Locate every Plasmodium parasite.
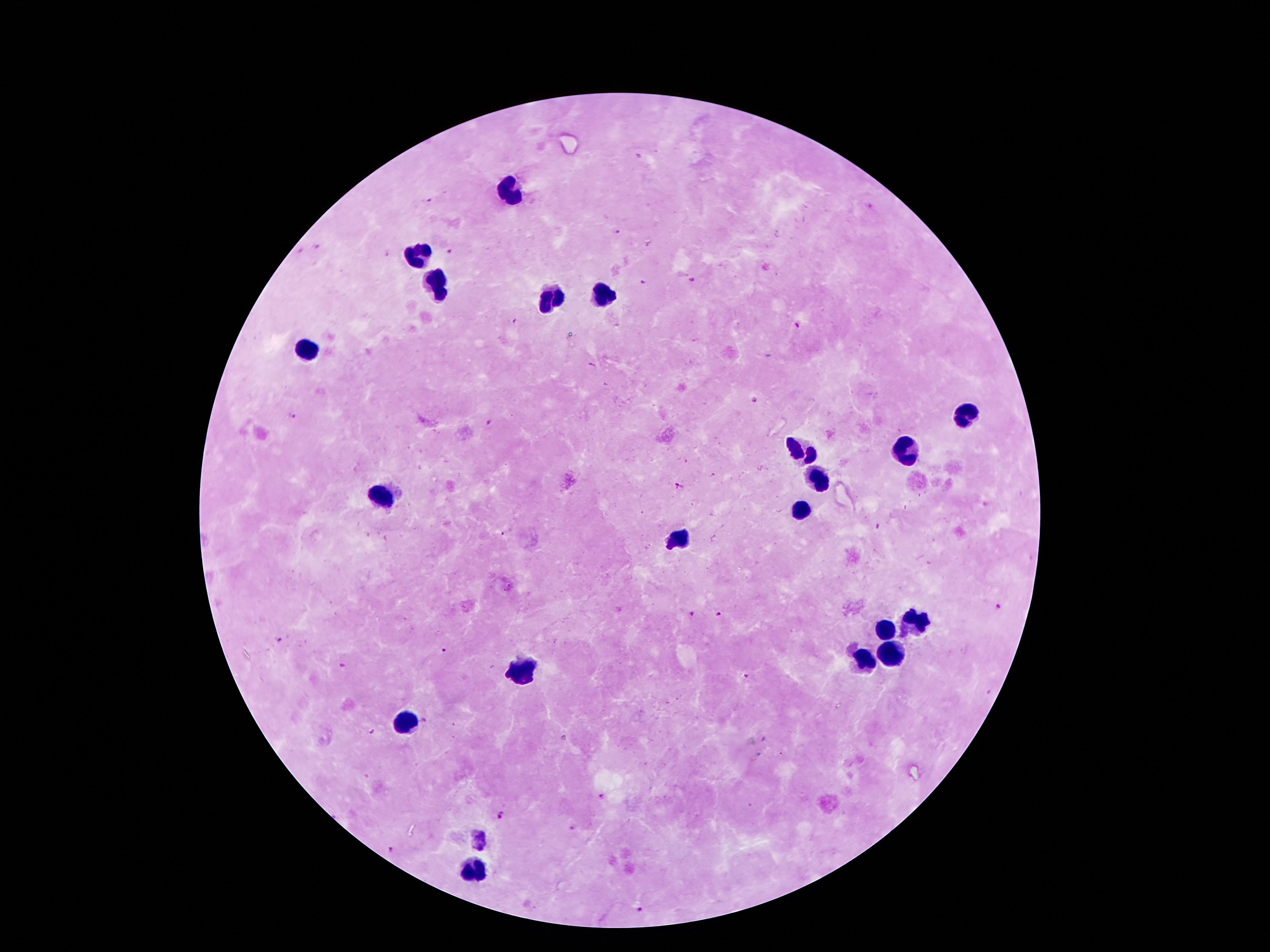
Approximate centers as [x, y] in pixels.
Plasmodium parasites: [428, 200], [872, 205], [618, 233], [319, 246], [300, 250], [449, 250], [385, 254], [691, 281], [644, 282], [513, 322], [796, 325], [591, 365], [754, 399], [292, 417], [489, 425], [678, 486], [877, 528], [508, 533], [998, 604], [718, 613], [691, 614], [280, 639], [446, 650], [343, 667], [747, 678], [989, 692], [424, 721], [372, 731], [780, 753], [599, 797], [751, 806], [501, 815], [574, 828], [390, 849], [640, 910].

Leukocyte locations: [508, 189], [419, 255], [438, 282], [603, 296], [547, 298], [308, 348], [964, 416], [801, 450], [905, 451], [819, 480], [381, 496], [799, 510], [680, 537], [910, 623], [885, 628], [891, 651], [864, 660], [521, 669], [408, 723], [476, 866]. Giemsa stain. Photographed through the microscope eyepiece with a smartphone camera. 100x magnification. Image is 1270×952 pixels. Thick blood film. Patient malaria status: infected with Plasmodium falciparum. One field from this slide.